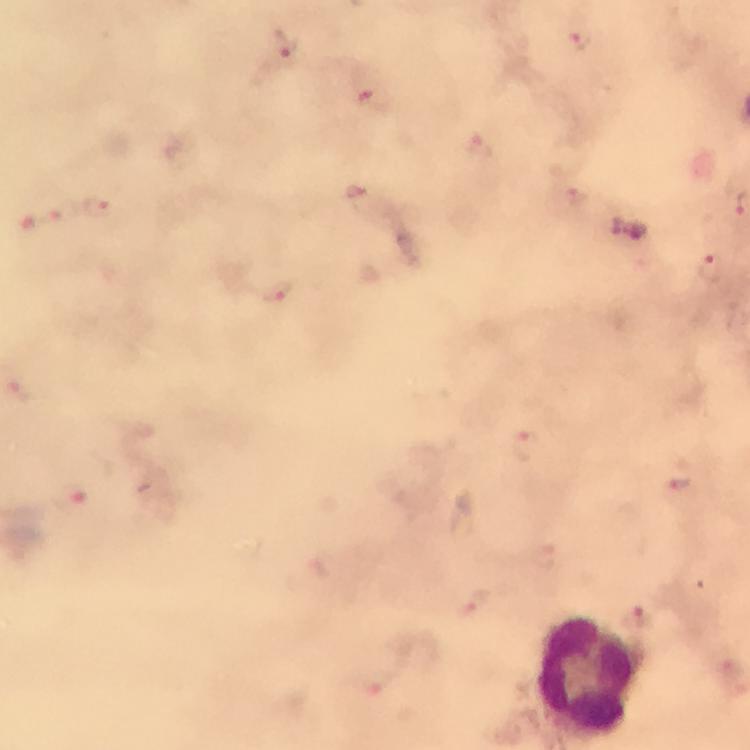

Approximate object centers, in pixels from the top-left corner. Plasmodium parasite locations: (x=581, y=42), (x=286, y=48), (x=373, y=103), (x=480, y=150), (x=358, y=189), (x=576, y=196), (x=96, y=205), (x=616, y=230), (x=634, y=232), (x=710, y=269), (x=275, y=291), (x=19, y=390), (x=526, y=447), (x=681, y=483), (x=75, y=491), (x=546, y=559), (x=470, y=605), (x=378, y=684). Leukocyte locations: (x=584, y=677). Cropped region of a single field of view. Image is 750×750 pixels. Giemsa-stained preparation. At 100x magnification. Immersion oil applied. Thick blood smear. From a diagnostic examination for malaria. Smartphone photograph taken through a microscope.